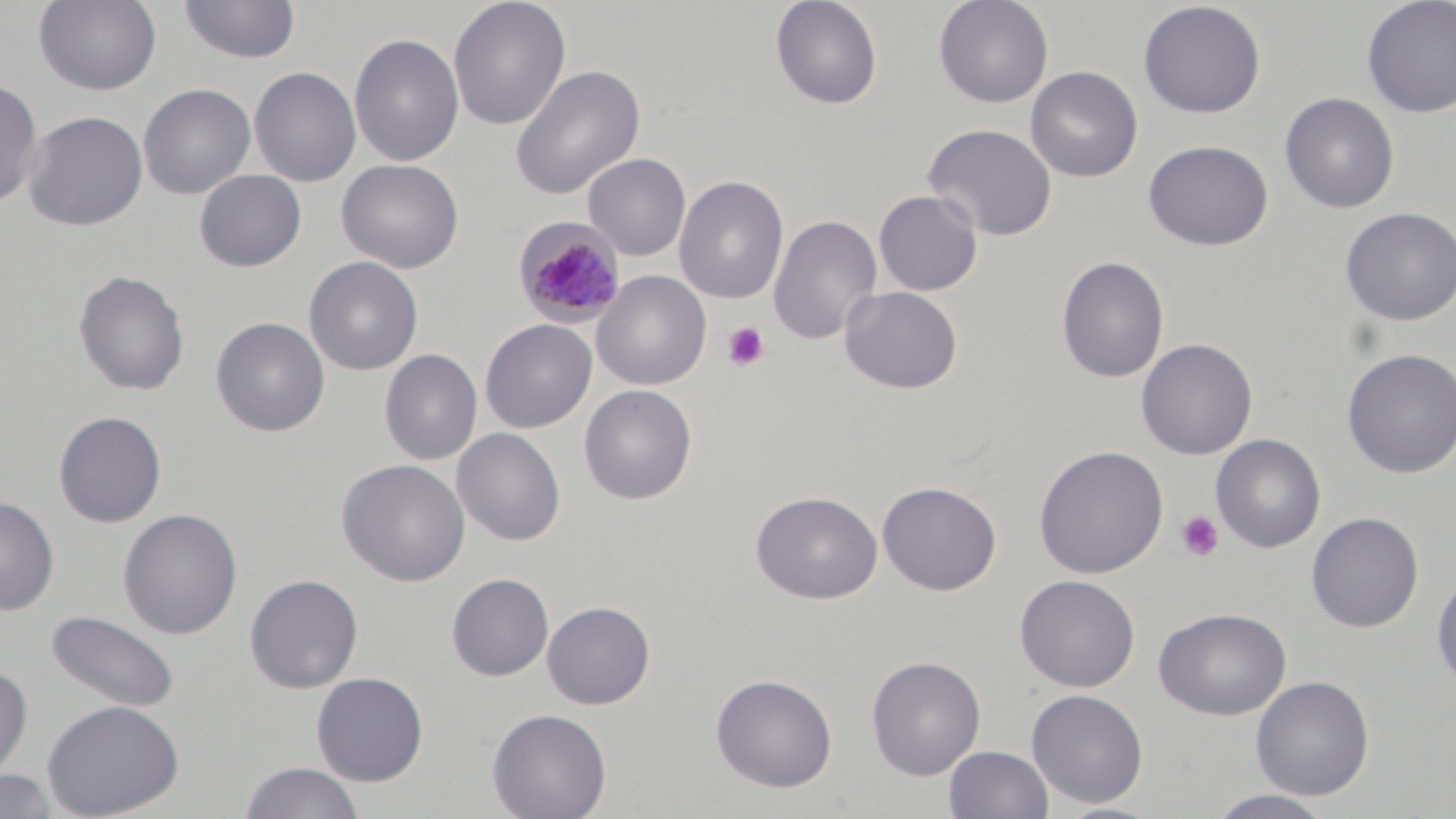
Approximate bounding boxes as (x1,y1)-(x2,y2) corner pairs in pixels. Uninfected red blood cell locations: (34,0)-(162,95), (448,0)-(571,131), (769,0)-(883,110), (933,0)-(1054,108), (1360,0)-(1456,117), (178,1)-(301,65), (1138,1)-(1266,119), (349,33)-(465,167), (510,65)-(645,200), (249,66)-(362,187), (1025,66)-(1143,182), (0,75)-(43,209), (138,83)-(256,198), (1279,92)-(1400,214), (23,110)-(148,232), (922,123)-(1058,242), (1143,140)-(1273,251), (583,153)-(691,260), (336,158)-(464,273), (194,170)-(306,272), (674,175)-(789,305), (873,189)-(983,296), (1340,207)-(1456,326), (769,214)-(882,346), (304,256)-(423,376), (1056,256)-(1169,382), (73,269)-(190,397), (592,270)-(712,390), (839,285)-(963,394), (210,316)-(330,437), (480,319)-(597,433), (1136,338)-(1257,459), (1341,347)-(1456,478), (379,349)-(482,466), (579,384)-(698,504), (53,411)-(167,528), (452,428)-(566,546), (1211,434)-(1326,553), (1033,445)-(1168,579), (335,459)-(471,587), (877,481)-(1002,595), (751,491)-(883,604), (0,496)-(59,615), (117,509)-(243,639), (1306,512)-(1424,633), (1431,569)-(1456,692), (245,573)-(363,693), (446,573)-(553,681), (1014,574)-(1140,692), (541,600)-(655,709), (1153,607)-(1292,720), (46,609)-(179,713), (866,656)-(986,779), (0,663)-(33,782), (311,672)-(428,786), (711,673)-(837,792), (1250,675)-(1375,801), (1026,689)-(1149,808), (41,698)-(185,819), (486,708)-(612,819), (944,745)-(1054,818), (239,761)-(365,819), (0,769)-(57,818), (1203,790)-(1339,819). Platelet locations: (721,321)-(770,371), (1175,510)-(1225,562). Plasmodium malariae-infected red blood cell locations: (514,217)-(626,326). Slide-level diagnosis: Plasmodium malariae. Image is 1456×819 pixels. Captured at 1000x magnification. One field of a larger specimen. Optical microscopy. May-Grünwald-Giemsa-stained preparation. Thin blood film.